Classify this cell by malaria status.
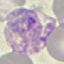

It is parasitized.

Acquired by smartphone through the microscope eyepiece. Thin smear of blood. Giemsa stain. Cell patch, automatically extracted from a larger field of view and resized to 64 × 64 pixels.